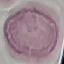 Result: negative for malaria parasites. Thin smear of blood. Photographed with a smartphone camera at the microscope eyepiece. Automatically extracted cell patch, resized to 64 × 64 pixels. Giemsa stain.